Comment on the morphology of the red blood cells.
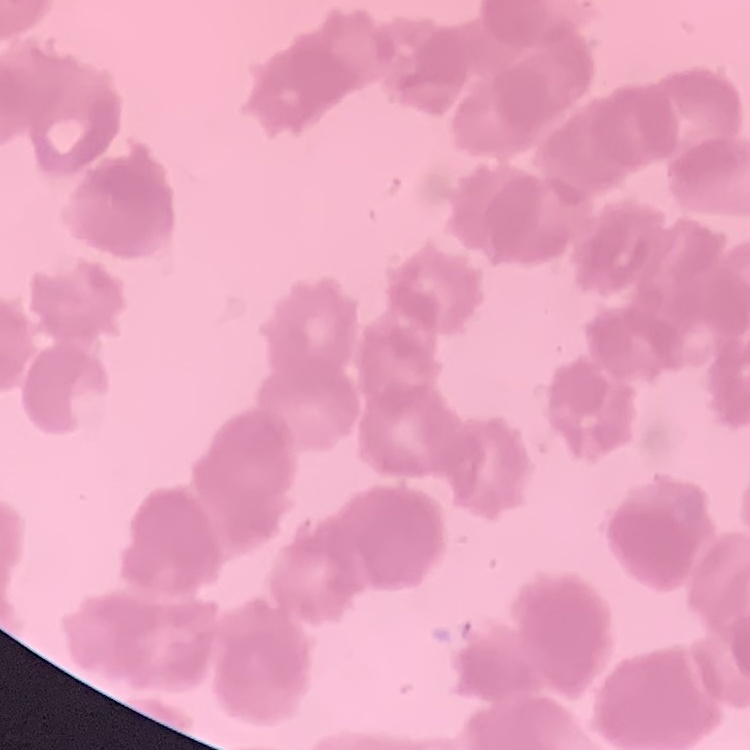

They show rouleaux formation.

Summary:
  - Stain: Field's or Giemsa
  - Image type: square crop of a larger photomicrograph
  - Preparation: thin blood film